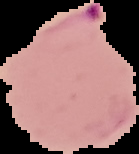 Malaria status: parasitized. From a thin blood film. Image is 139×154 pixels. The area outside the segmented cell region is set to black.